Name the parasite shown.
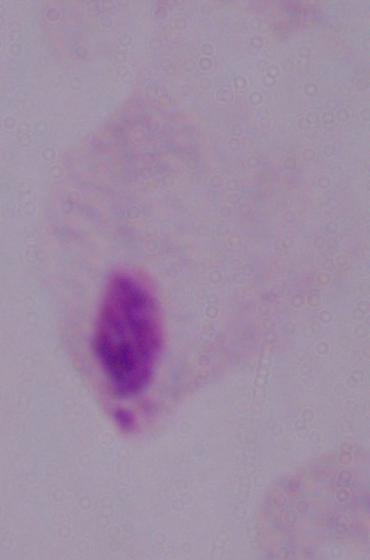
A trichomonad.

Captured at 1000x magnification. Photomicrograph.